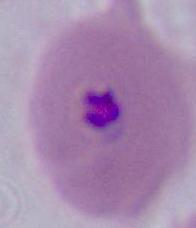
Summary:
  - Identification: Plasmodium
  - Modality: photomicrograph
  - Magnification: 400x or 1000x